Point out each malaria parasite.
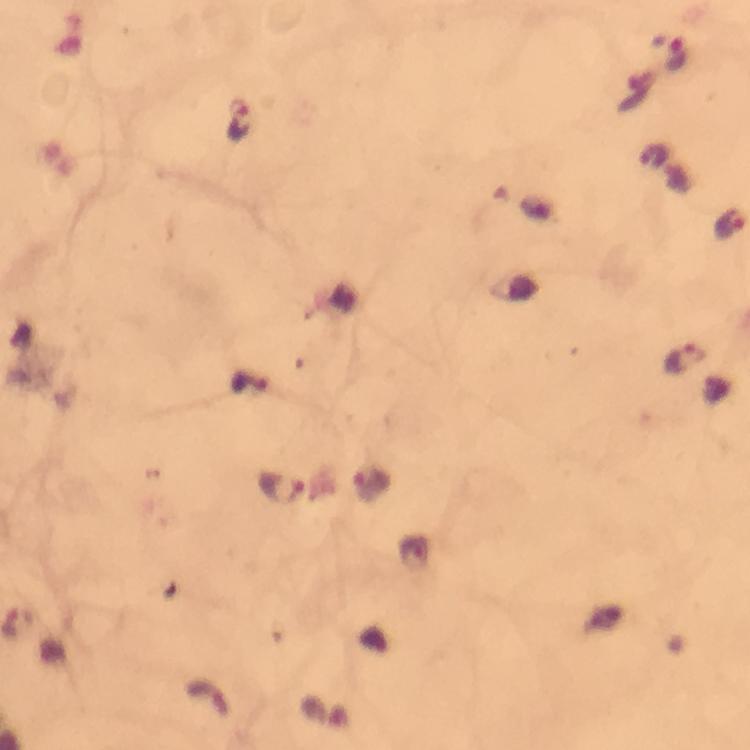
Approximate centers as [x, y] in pixels.
Malaria parasites: [240, 123], [730, 226], [686, 357], [279, 489].

{
  "cropped_from": "one field of view",
  "image_size": "750×750 pixels",
  "magnification": "100x",
  "preparation": "thick smear",
  "immersion_oil": "applied",
  "capture": "smartphone camera through the microscope",
  "stain": "Giemsa",
  "context": "from a malaria diagnostic workup"
}